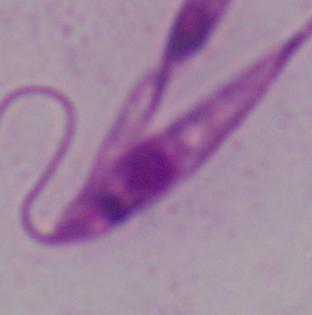
{
  "identification": "Leishmania",
  "magnification": "1000x",
  "modality": "micrograph"
}